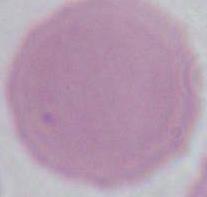

modality = photomicrograph
magnification = 1000x
identification = red blood cell